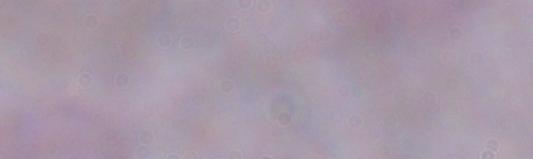
{
  "identification": "trypanosome",
  "modality": "photomicrograph",
  "magnification": "1000x"
}